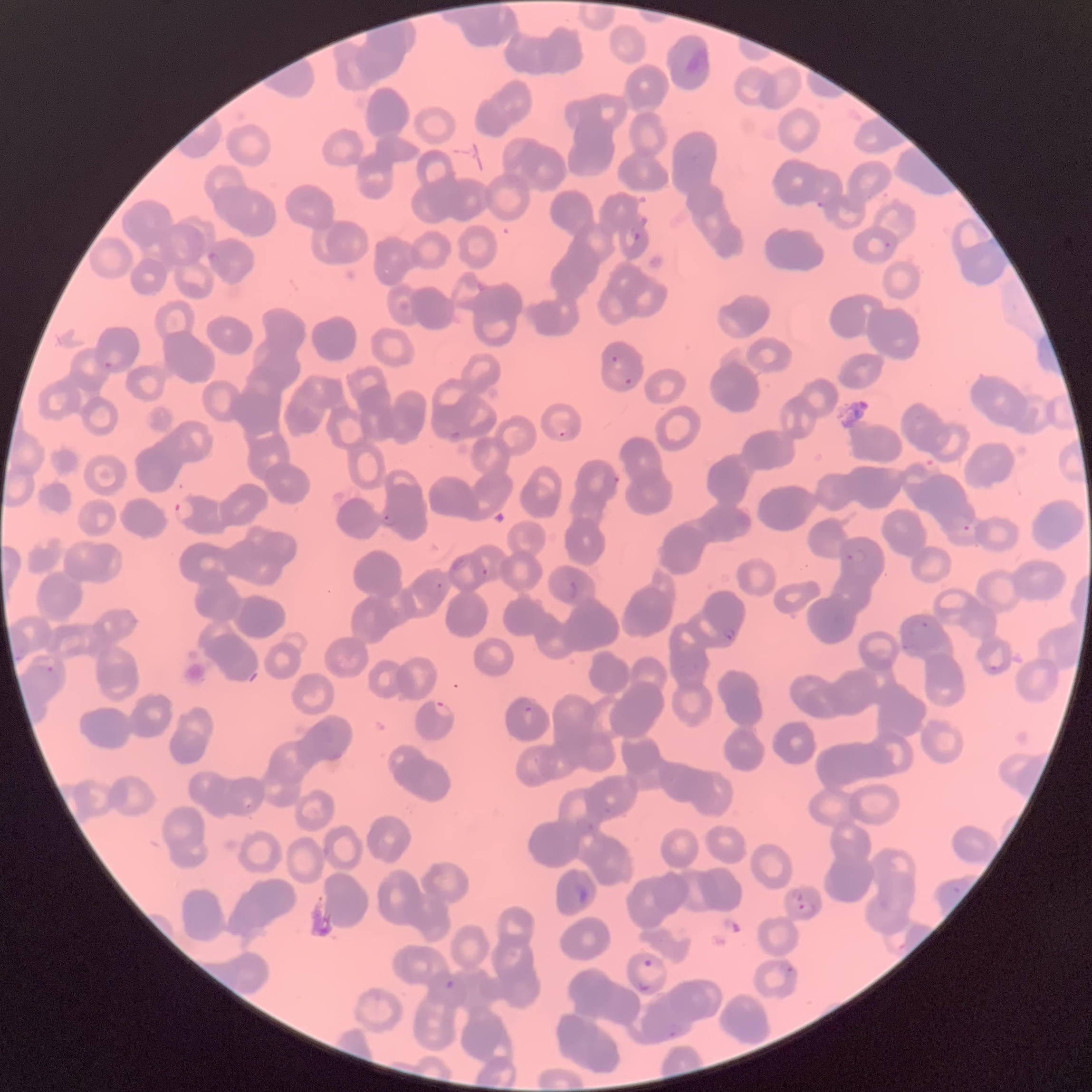

coordinate format = approximate bounding boxes as (x1, y1, x2, y2) in pixels
Plasmodium parasites too small for a box (approximate centers as (x, y) in pixels) = (440, 585)
Plasmodium parasite locations = (817, 200, 824, 209), (631, 232, 640, 241), (884, 241, 891, 249), (206, 251, 222, 263), (610, 355, 619, 363), (101, 360, 114, 371), (623, 377, 633, 386), (449, 431, 460, 441), (558, 431, 566, 437), (918, 457, 939, 474), (613, 475, 620, 484), (173, 497, 196, 524), (382, 514, 396, 527), (961, 523, 971, 532), (845, 547, 869, 566), (481, 568, 489, 576), (570, 581, 577, 599), (912, 619, 932, 629), (722, 626, 736, 641), (902, 638, 915, 652), (988, 662, 1002, 671), (46, 665, 54, 673), (432, 700, 452, 719), (522, 705, 535, 725), (575, 882, 587, 901), (796, 892, 806, 902), (797, 901, 818, 917), (642, 958, 654, 968), (785, 965, 795, 975), (445, 978, 455, 989), (638, 981, 653, 994), (667, 1022, 684, 1038)
preparation = thin blood film
image size = 1092×1092 pixels
red blood cell morphology = rouleaux formation
modality = light microscopy